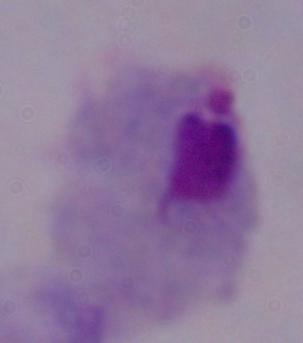

A trichomonad is seen. Captured at 1000x magnification. Photomicrograph.